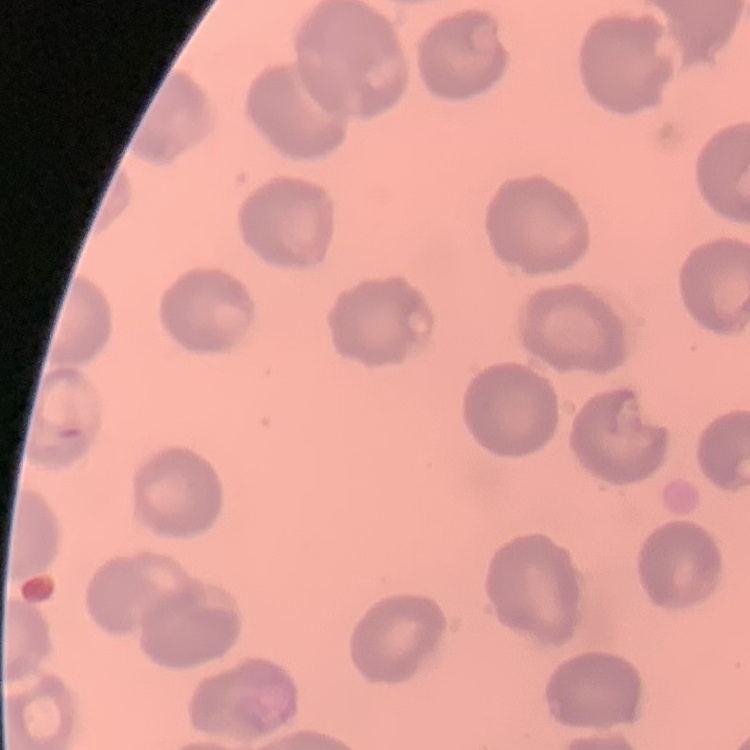
erythrocyte morphology = no rouleaux formation
stain = Field's or Giemsa
preparation = thin blood smear
image type = square crop of a larger photomicrograph